Identify the blood parasite species.
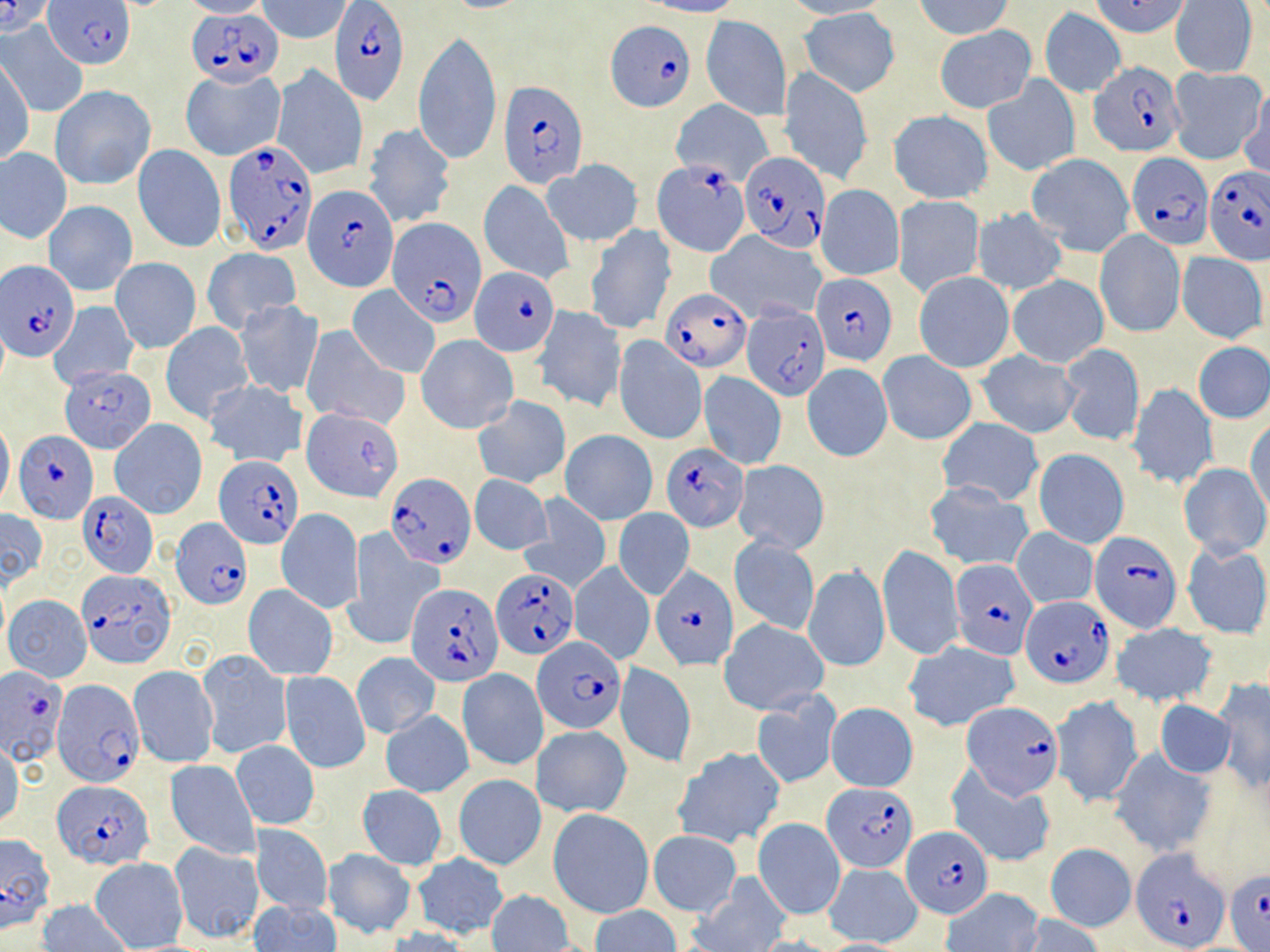
Plasmodium falciparum.

Approximate bounding boxes as named x1/y1/x2/y2 corners in pixels. Uninfected red blood cell locations (subset): (x1=180, y1=0, x2=268, y2=18), (x1=261, y1=0, x2=352, y2=42), (x1=642, y1=0, x2=743, y2=18), (x1=780, y1=0, x2=894, y2=20), (x1=916, y1=0, x2=1015, y2=40), (x1=1090, y1=0, x2=1192, y2=38), (x1=1171, y1=1, x2=1257, y2=78), (x1=799, y1=7, x2=900, y2=96), (x1=1040, y1=8, x2=1125, y2=96), (x1=701, y1=14, x2=792, y2=121), (x1=1, y1=22, x2=87, y2=116), (x1=934, y1=25, x2=1037, y2=115), (x1=414, y1=28, x2=503, y2=165), (x1=2, y1=57, x2=33, y2=163), (x1=271, y1=65, x2=368, y2=181), (x1=1167, y1=67, x2=1266, y2=166), (x1=781, y1=68, x2=872, y2=184), (x1=181, y1=69, x2=285, y2=161), (x1=983, y1=76, x2=1080, y2=175), (x1=1241, y1=82, x2=1270, y2=181), (x1=50, y1=84, x2=156, y2=190), (x1=670, y1=100, x2=773, y2=185), (x1=888, y1=111, x2=993, y2=203), (x1=362, y1=122, x2=456, y2=229), (x1=133, y1=144, x2=225, y2=252), (x1=0, y1=147, x2=72, y2=243), (x1=1027, y1=154, x2=1135, y2=257), (x1=544, y1=160, x2=642, y2=246), (x1=479, y1=180, x2=571, y2=283), (x1=816, y1=184, x2=904, y2=280), (x1=891, y1=194, x2=984, y2=297), (x1=42, y1=200, x2=137, y2=296), (x1=973, y1=207, x2=1068, y2=297), (x1=584, y1=225, x2=676, y2=333), (x1=1094, y1=229, x2=1185, y2=337), (x1=707, y1=230, x2=826, y2=323), (x1=202, y1=246, x2=301, y2=334), (x1=1177, y1=252, x2=1268, y2=343), (x1=111, y1=258, x2=201, y2=352), (x1=915, y1=271, x2=1014, y2=372), (x1=1008, y1=275, x2=1108, y2=367), (x1=348, y1=285, x2=440, y2=378), (x1=49, y1=301, x2=139, y2=388), (x1=235, y1=301, x2=322, y2=399), (x1=532, y1=305, x2=626, y2=414), (x1=161, y1=322, x2=253, y2=424), (x1=300, y1=327, x2=407, y2=430), (x1=416, y1=334, x2=519, y2=434), (x1=613, y1=337, x2=707, y2=445), (x1=1193, y1=342, x2=1270, y2=423), (x1=1057, y1=343, x2=1144, y2=447), (x1=977, y1=351, x2=1081, y2=438), (x1=878, y1=352, x2=976, y2=445), (x1=802, y1=363, x2=892, y2=461), (x1=698, y1=371, x2=786, y2=468), (x1=203, y1=379, x2=308, y2=468), (x1=1125, y1=384, x2=1219, y2=491), (x1=474, y1=396, x2=570, y2=488), (x1=307, y1=407, x2=404, y2=503), (x1=0, y1=417, x2=14, y2=510), (x1=110, y1=419, x2=207, y2=518), (x1=937, y1=419, x2=1043, y2=506), (x1=1246, y1=420, x2=1270, y2=519), (x1=561, y1=430, x2=657, y2=523), (x1=1033, y1=448, x2=1129, y2=548), (x1=734, y1=460, x2=829, y2=553), (x1=1178, y1=463, x2=1269, y2=557), (x1=470, y1=473, x2=553, y2=555), (x1=923, y1=485, x2=1034, y2=572), (x1=519, y1=494, x2=612, y2=592), (x1=0, y1=509, x2=48, y2=587), (x1=277, y1=509, x2=363, y2=614), (x1=613, y1=509, x2=694, y2=600), (x1=1012, y1=529, x2=1097, y2=609), (x1=345, y1=530, x2=443, y2=650), (x1=730, y1=536, x2=820, y2=636), (x1=1181, y1=542, x2=1270, y2=639), (x1=878, y1=544, x2=962, y2=660), (x1=570, y1=562, x2=654, y2=665), (x1=803, y1=565, x2=889, y2=673), (x1=244, y1=585, x2=336, y2=679), (x1=4, y1=595, x2=92, y2=681), (x1=721, y1=620, x2=828, y2=714), (x1=1113, y1=623, x2=1217, y2=706), (x1=903, y1=642, x2=1019, y2=733), (x1=197, y1=649, x2=291, y2=759), (x1=352, y1=652, x2=440, y2=738), (x1=613, y1=663, x2=697, y2=768), (x1=129, y1=666, x2=218, y2=767), (x1=457, y1=670, x2=547, y2=770), (x1=279, y1=671, x2=369, y2=774), (x1=1212, y1=678, x2=1270, y2=793), (x1=752, y1=694, x2=839, y2=788), (x1=1050, y1=695, x2=1143, y2=809), (x1=1154, y1=698, x2=1236, y2=779), (x1=826, y1=703, x2=918, y2=792), (x1=381, y1=709, x2=473, y2=797), (x1=533, y1=724, x2=632, y2=818), (x1=230, y1=739, x2=320, y2=830), (x1=0, y1=740, x2=22, y2=830), (x1=673, y1=747, x2=784, y2=848), (x1=1108, y1=748, x2=1217, y2=858), (x1=165, y1=760, x2=260, y2=859), (x1=948, y1=766, x2=1057, y2=868), (x1=453, y1=774, x2=546, y2=870), (x1=357, y1=785, x2=446, y2=869), (x1=548, y1=807, x2=655, y2=919), (x1=754, y1=818, x2=845, y2=920), (x1=251, y1=825, x2=332, y2=917), (x1=647, y1=831, x2=742, y2=917), (x1=170, y1=842, x2=263, y2=942), (x1=1045, y1=843, x2=1137, y2=932), (x1=322, y1=849, x2=417, y2=938), (x1=411, y1=853, x2=510, y2=938), (x1=90, y1=857, x2=188, y2=951), (x1=825, y1=864, x2=922, y2=946), (x1=688, y1=874, x2=790, y2=952), (x1=939, y1=887, x2=1043, y2=952), (x1=486, y1=889, x2=576, y2=952), (x1=37, y1=898, x2=131, y2=952), (x1=248, y1=898, x2=341, y2=952), (x1=590, y1=905, x2=679, y2=952), (x1=1017, y1=913, x2=1103, y2=951), (x1=384, y1=927, x2=478, y2=952), (x1=813, y1=939, x2=912, y2=951). Plasmodium falciparum-infected red blood cell locations (subset): (x1=0, y1=0, x2=56, y2=36), (x1=329, y1=0, x2=408, y2=104), (x1=44, y1=1, x2=136, y2=69), (x1=187, y1=8, x2=282, y2=87), (x1=605, y1=20, x2=695, y2=113), (x1=1088, y1=60, x2=1186, y2=158), (x1=499, y1=81, x2=588, y2=189), (x1=223, y1=137, x2=319, y2=255), (x1=740, y1=152, x2=830, y2=251), (x1=1124, y1=152, x2=1212, y2=253), (x1=652, y1=163, x2=752, y2=257), (x1=1203, y1=164, x2=1269, y2=265), (x1=303, y1=183, x2=399, y2=292), (x1=389, y1=218, x2=488, y2=326), (x1=3, y1=261, x2=80, y2=362), (x1=471, y1=266, x2=559, y2=358), (x1=812, y1=272, x2=897, y2=366), (x1=660, y1=288, x2=751, y2=371), (x1=742, y1=306, x2=830, y2=401), (x1=61, y1=365, x2=156, y2=453), (x1=15, y1=431, x2=98, y2=524), (x1=661, y1=443, x2=749, y2=531), (x1=385, y1=473, x2=477, y2=568), (x1=80, y1=492, x2=157, y2=575), (x1=171, y1=516, x2=250, y2=609), (x1=1092, y1=532, x2=1182, y2=633), (x1=950, y1=560, x2=1038, y2=659), (x1=650, y1=566, x2=737, y2=670), (x1=490, y1=568, x2=578, y2=658), (x1=76, y1=571, x2=176, y2=667), (x1=406, y1=582, x2=503, y2=686), (x1=1023, y1=596, x2=1112, y2=687), (x1=533, y1=639, x2=625, y2=734), (x1=2, y1=670, x2=70, y2=766), (x1=50, y1=680, x2=141, y2=787), (x1=960, y1=702, x2=1064, y2=801), (x1=52, y1=781, x2=155, y2=869), (x1=822, y1=781, x2=918, y2=872), (x1=901, y1=826, x2=994, y2=918), (x1=0, y1=832, x2=56, y2=930), (x1=1132, y1=846, x2=1231, y2=950). Thin blood smear. Captured at 1000x magnification. Light microscopy. One field of a larger specimen. May-Grünwald-Giemsa stain. Image is 1270×952 pixels.